Name the parasite shown.
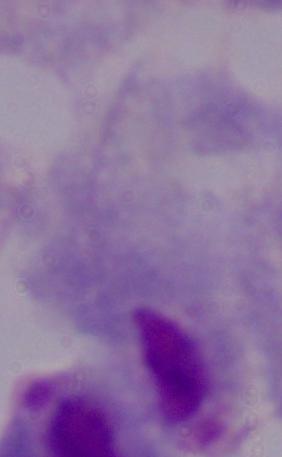
This is a trichomonad.

Summary:
  - Magnification: 1000x
  - Modality: micrograph